Comment on the morphology of the erythrocytes.
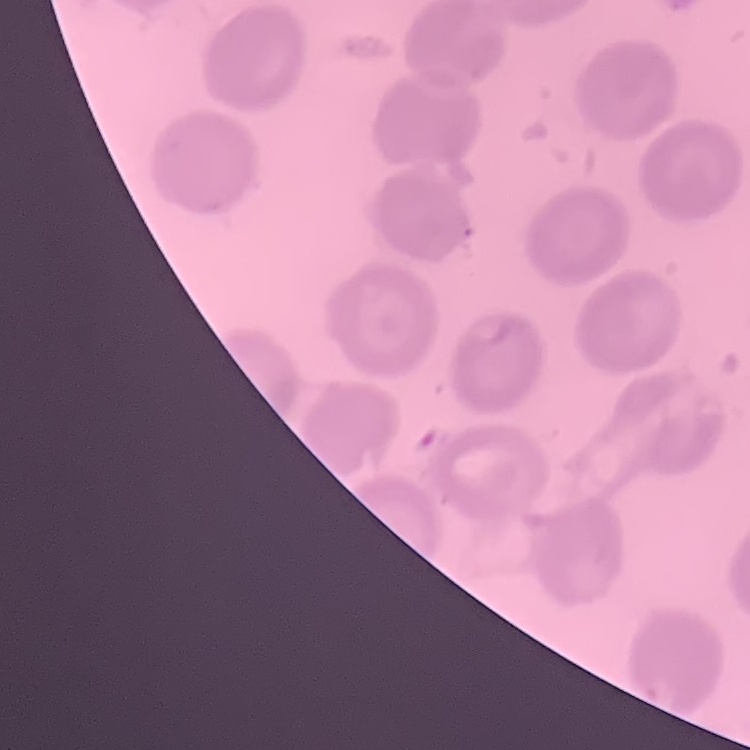
They show no rouleaux formation.

{
  "image_type": "one tile cut from a larger photomicrograph",
  "preparation": "thin blood smear",
  "stain": "Field's or Giemsa"
}